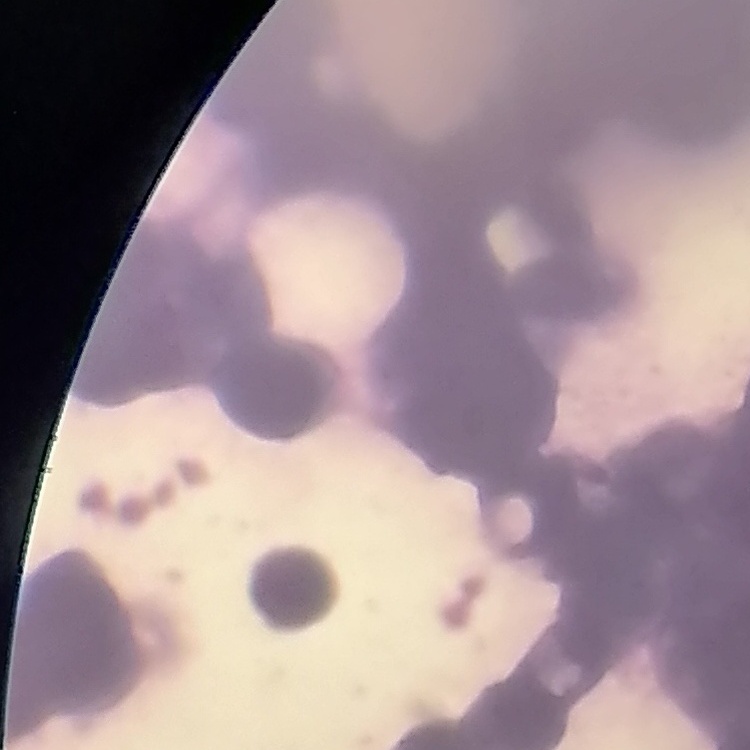

The erythrocytes show rouleaux formation. Square crop of a larger photomicrograph. Thin blood smear. Stained with either Field's or Giemsa.